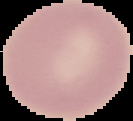 Image is 133×121 pixels. Cell region segmented out of the field of view; the surrounding area is masked to black. Result: no malaria parasites detected. From a thin blood smear.